Report the malaria status of this cell.
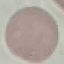
Uninfected.

stain = Giemsa
capture = smartphone through the microscope eyepiece
image type = cell patch, automatically extracted from a larger field of view and resized to 64 × 64 pixels
preparation = thin blood smear